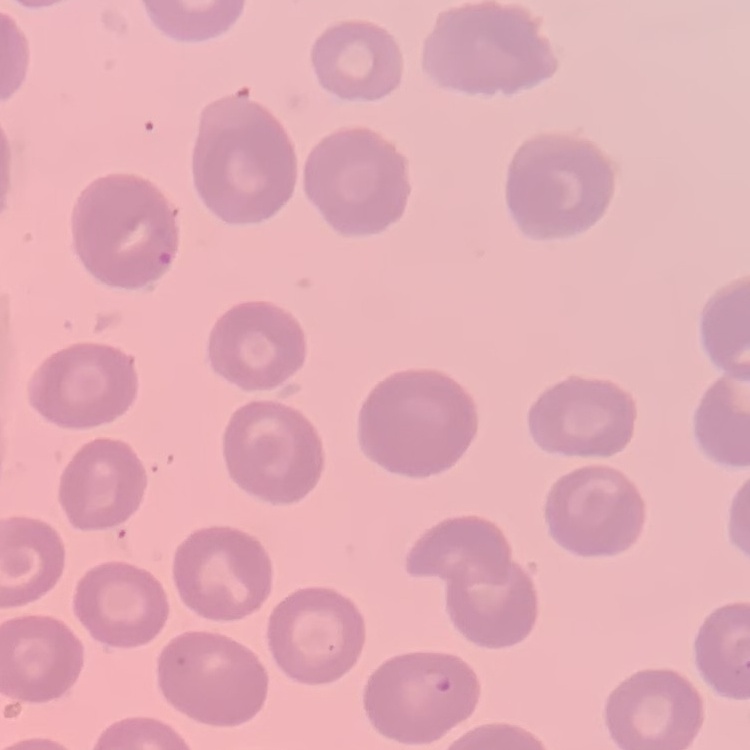

The erythrocytes show no rouleaux formation. Stained with either Field's or Giemsa. One tile cut from a larger photomicrograph. Thin blood film.